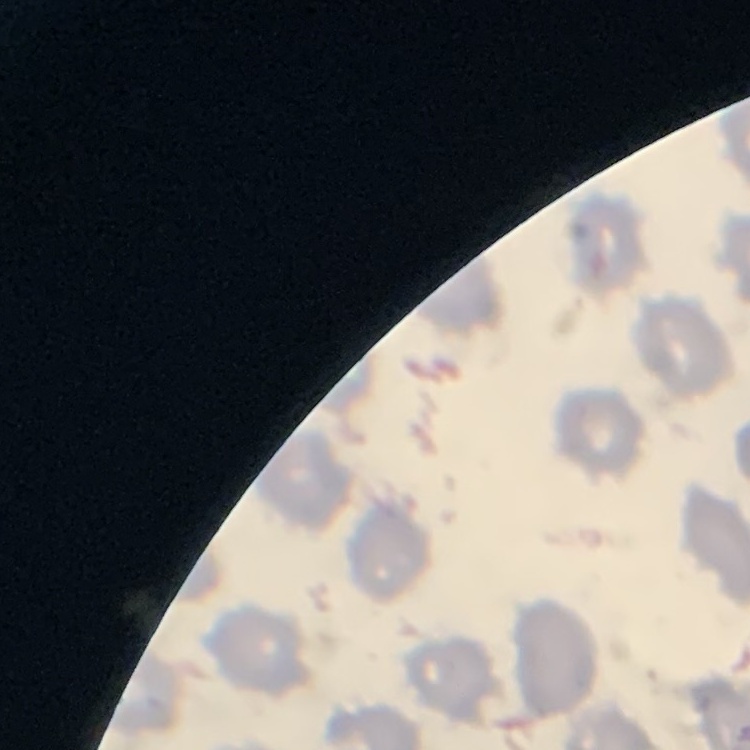 The red blood cells show no rouleaux formation. Thin peripheral smear. Square crop of a larger photomicrograph. Stained with either Field's or Giemsa.